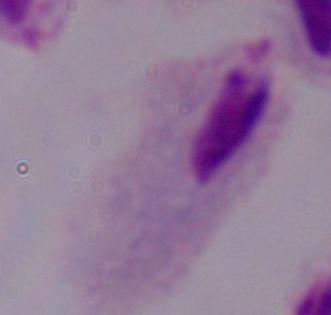
Micrograph. 1000x magnification. A trichomonad is seen.